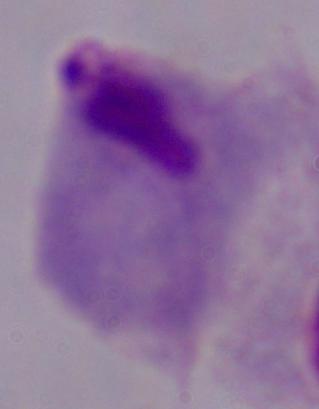
Summary:
  - Magnification: 1000x
  - Identification: trichomonad
  - Modality: micrograph